Assess the morphology of the erythrocytes.
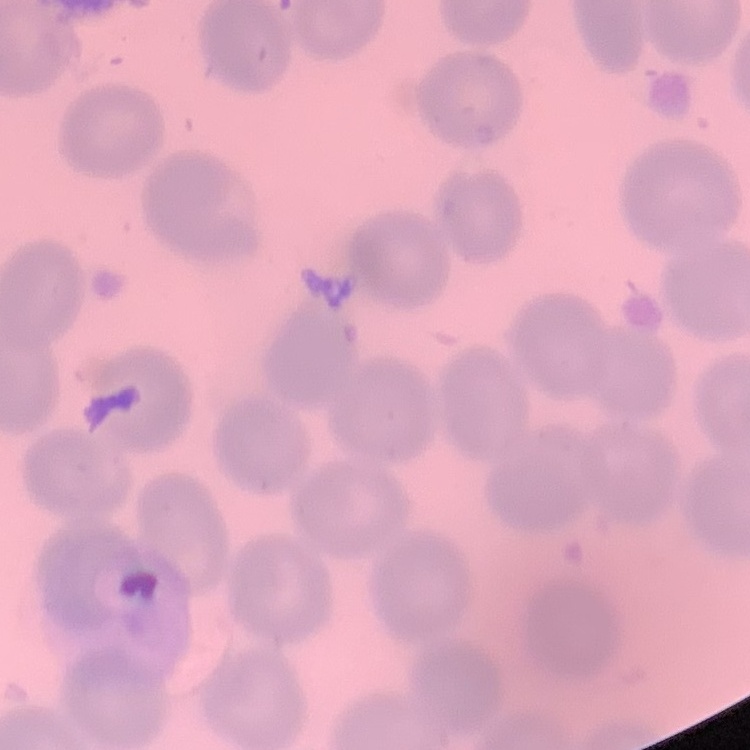

They show no rouleaux formation.

Summary:
  - Stain: Field's or Giemsa
  - Preparation: thin blood film
  - Image type: square crop of a larger photomicrograph